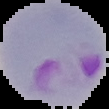

Cell region segmented out of the field of view; the surrounding area is masked to black. Result: malaria parasites identified. Image is 109×109 pixels. From a thin blood smear.